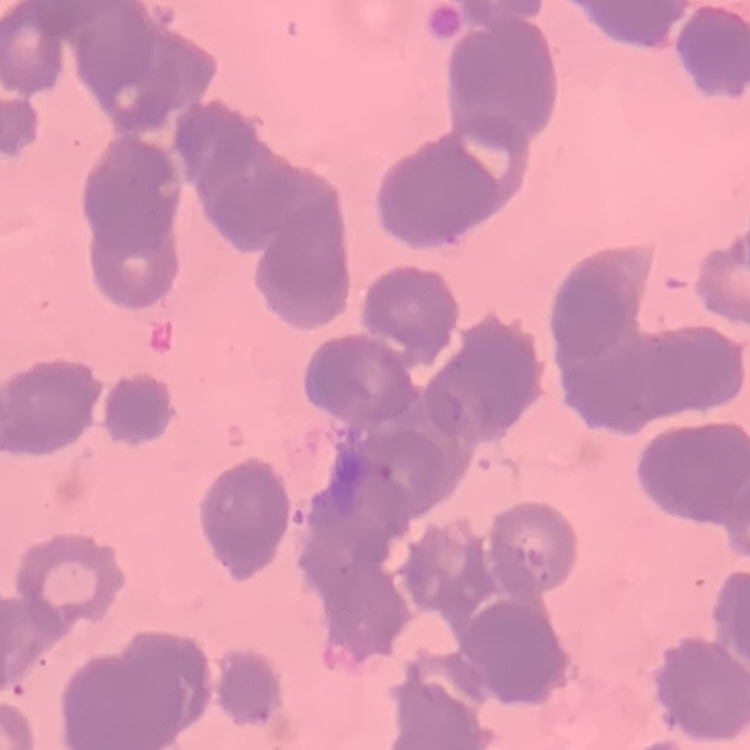

Summary:
  - Erythrocyte morphology: rouleaux formation
  - Stain: Field's or Giemsa
  - Image type: one tile cut from a larger photomicrograph
  - Preparation: thin peripheral smear